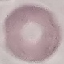

Summary:
  - Result: no malaria parasites detected
  - Stain: Giemsa
  - Image type: cell patch, automatically extracted from a larger field of view and resized to 64 × 64 pixels
  - Capture: smartphone through the microscope eyepiece
  - Preparation: thin smear